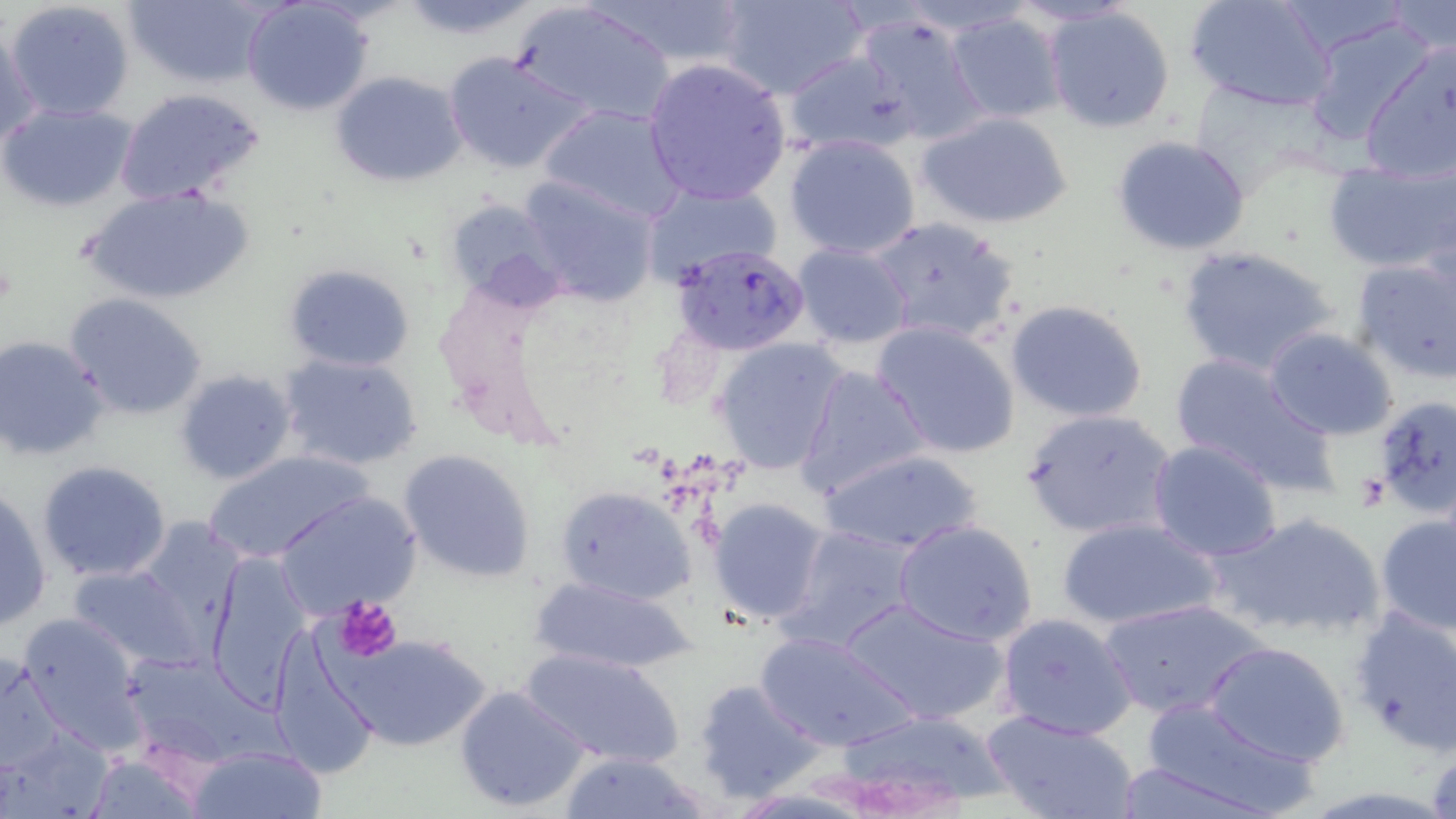
slide-level diagnosis = Plasmodium falciparum
preparation = thin blood film
field of view = one of a larger specimen
uninfected red blood cell locations = approximate bounding boxes as (x1, y1, x2, y2) in pixels: (5, 0, 136, 121), (125, 0, 264, 87), (603, 0, 754, 66), (718, 0, 866, 100), (1005, 0, 1141, 29), (512, 1, 675, 127), (1187, 1, 1336, 112), (241, 2, 372, 118), (1386, 3, 1455, 59), (1044, 6, 1177, 133), (944, 9, 1068, 123), (854, 14, 989, 146), (1301, 14, 1436, 146), (0, 28, 43, 148), (1360, 44, 1456, 183), (443, 51, 591, 175), (782, 51, 917, 156), (642, 56, 791, 205), (330, 70, 467, 187), (114, 85, 265, 207), (0, 103, 135, 210), (540, 103, 687, 222), (918, 111, 1073, 229), (785, 133, 921, 261), (1110, 135, 1251, 256), (1323, 164, 1456, 273), (517, 173, 660, 305), (640, 178, 782, 284), (81, 186, 255, 306), (445, 198, 566, 304), (870, 215, 1024, 348), (791, 243, 913, 349), (1175, 244, 1343, 377), (1350, 252, 1455, 383), (284, 264, 414, 371), (63, 294, 206, 420), (1006, 301, 1149, 423), (872, 321, 1019, 459), (1262, 328, 1399, 440), (2, 335, 112, 462), (714, 337, 847, 474), (278, 353, 422, 470), (1168, 353, 1338, 494), (793, 364, 932, 500), (174, 369, 297, 486), (1370, 394, 1456, 517), (1021, 407, 1179, 540), (1146, 440, 1284, 562), (819, 449, 984, 555), (204, 450, 368, 566), (398, 450, 536, 581), (35, 460, 173, 584), (556, 486, 695, 604), (0, 489, 51, 630), (276, 491, 423, 617), (709, 498, 829, 625), (1204, 511, 1387, 643), (1375, 513, 1456, 637), (1058, 518, 1223, 631), (895, 520, 1039, 648), (134, 521, 248, 646), (778, 524, 922, 654), (207, 551, 312, 702), (68, 564, 200, 669), (526, 572, 698, 674), (839, 595, 1009, 725), (1097, 598, 1269, 720), (1347, 601, 1456, 757), (17, 610, 147, 753), (995, 613, 1137, 740), (753, 629, 919, 753), (330, 633, 489, 751), (271, 637, 377, 779), (1202, 640, 1351, 768), (520, 646, 684, 770), (1, 649, 64, 773), (693, 678, 824, 803), (454, 684, 591, 813), (1138, 699, 1318, 818), (828, 709, 1008, 810), (981, 709, 1139, 819), (187, 744, 327, 819), (560, 750, 710, 819), (85, 753, 206, 818), (1113, 761, 1269, 818)
Plasmodium falciparum-infected red blood cell locations = approximate bounding boxes as (x1, y1, x2, y2) in pixels: (672, 243, 810, 354)
platelet locations = approximate bounding boxes as (x1, y1, x2, y2) in pixels: (334, 598, 403, 659)
magnification = 1000x
image size = 1456×819 pixels
stain = May-Grünwald-Giemsa
modality = optical microscopy